Name the cell type shown.
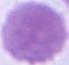

An erythrocyte.

{
  "modality": "photomicrograph",
  "magnification": "1000x"
}